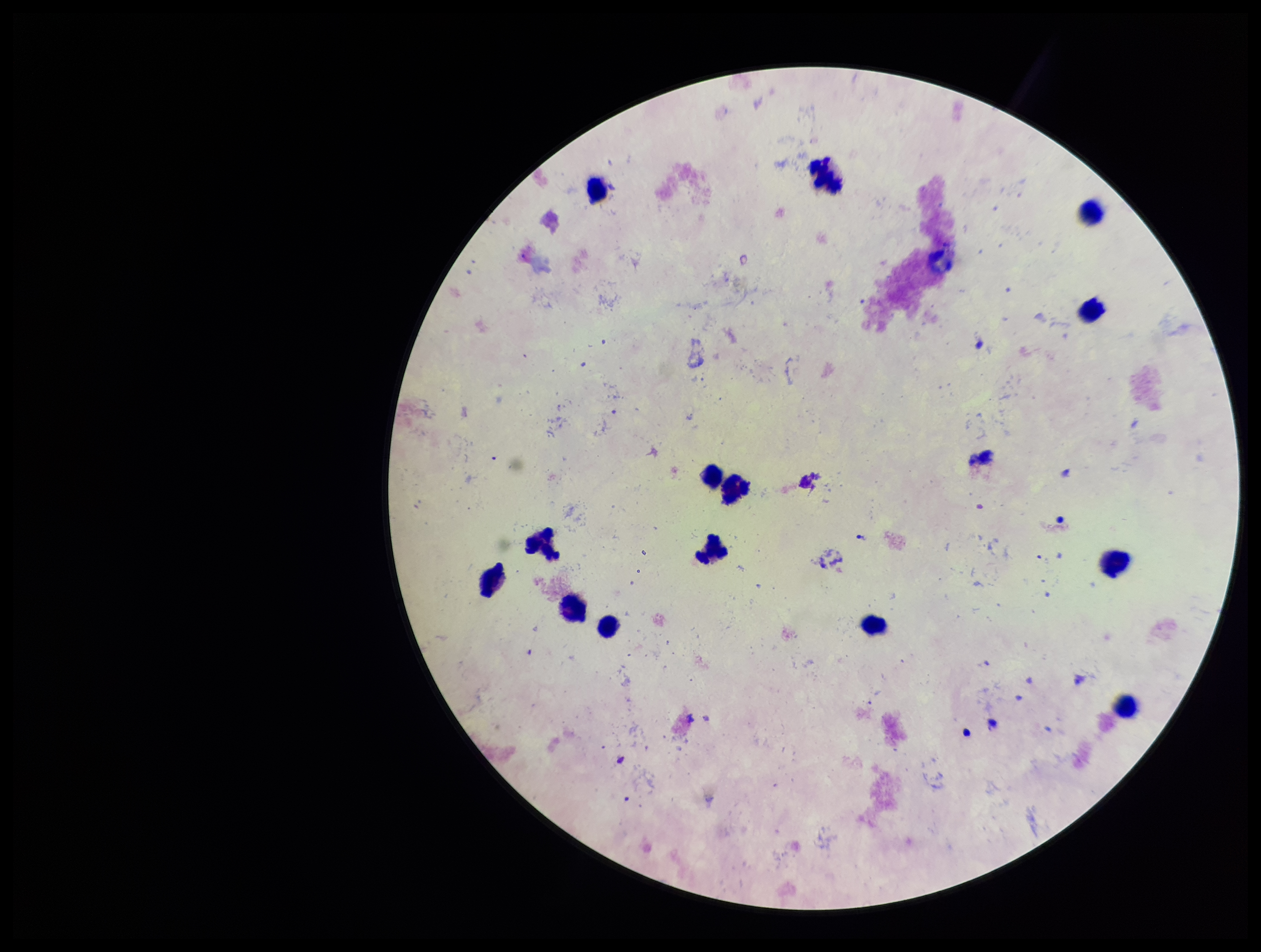
Summary:
  - Field of view: one from this slide
  - Parasite count: 0
  - Patient malaria status: negative
  - Leukocyte count: 14
  - Image size: 1261×952 pixels
  - Plasmodium parasites: none seen
  - Stain: Giemsa
  - Preparation: thick smear
  - Capture: smartphone photograph through the microscope eyepiece